Locate leukocytes (white blood cells).
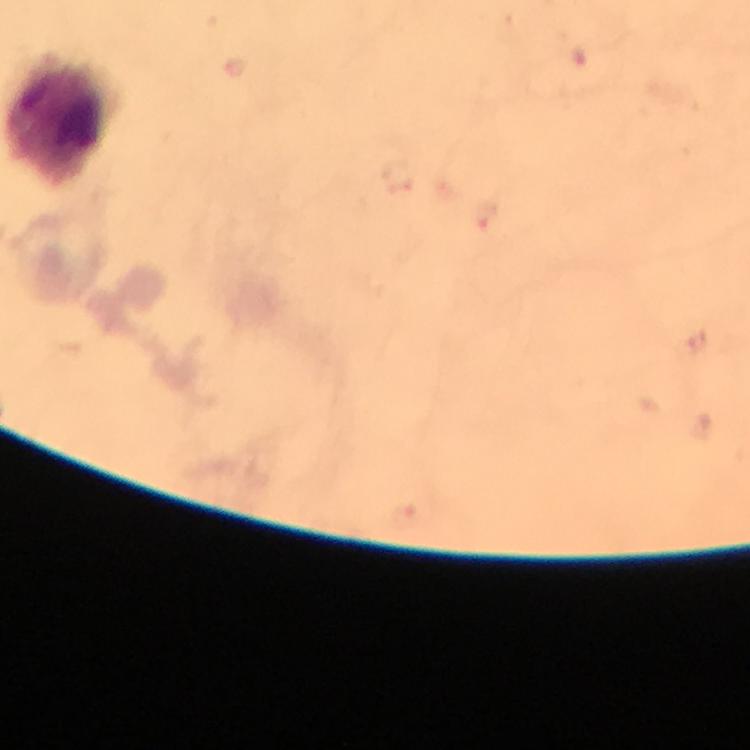
Approximate object centers, in pixels from the top-left corner.
Leukocytes: (x=60, y=121).

Photographed with a smartphone mounted on the microscope. Thick blood smear. From a malaria diagnostic workup. Image is 750×750 pixels. A crop from one field of view. Malaria parasites: none seen. Giemsa-stained preparation. Immersion oil was used. At 100x magnification.